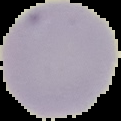 From a thin blood smear. The area outside the segmented cell region is set to black. Result: negative for Plasmodium parasites. Image is 121×121 pixels.